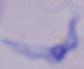

modality = photomicrograph
magnification = 1000x
identification = trypanosome